Report the malaria status of this cell.
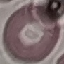
It is uninfected.

capture = smartphone through the microscope eyepiece
stain = Giemsa
image type = automatically extracted cell patch, resized to 64 × 64 pixels
preparation = thin blood smear